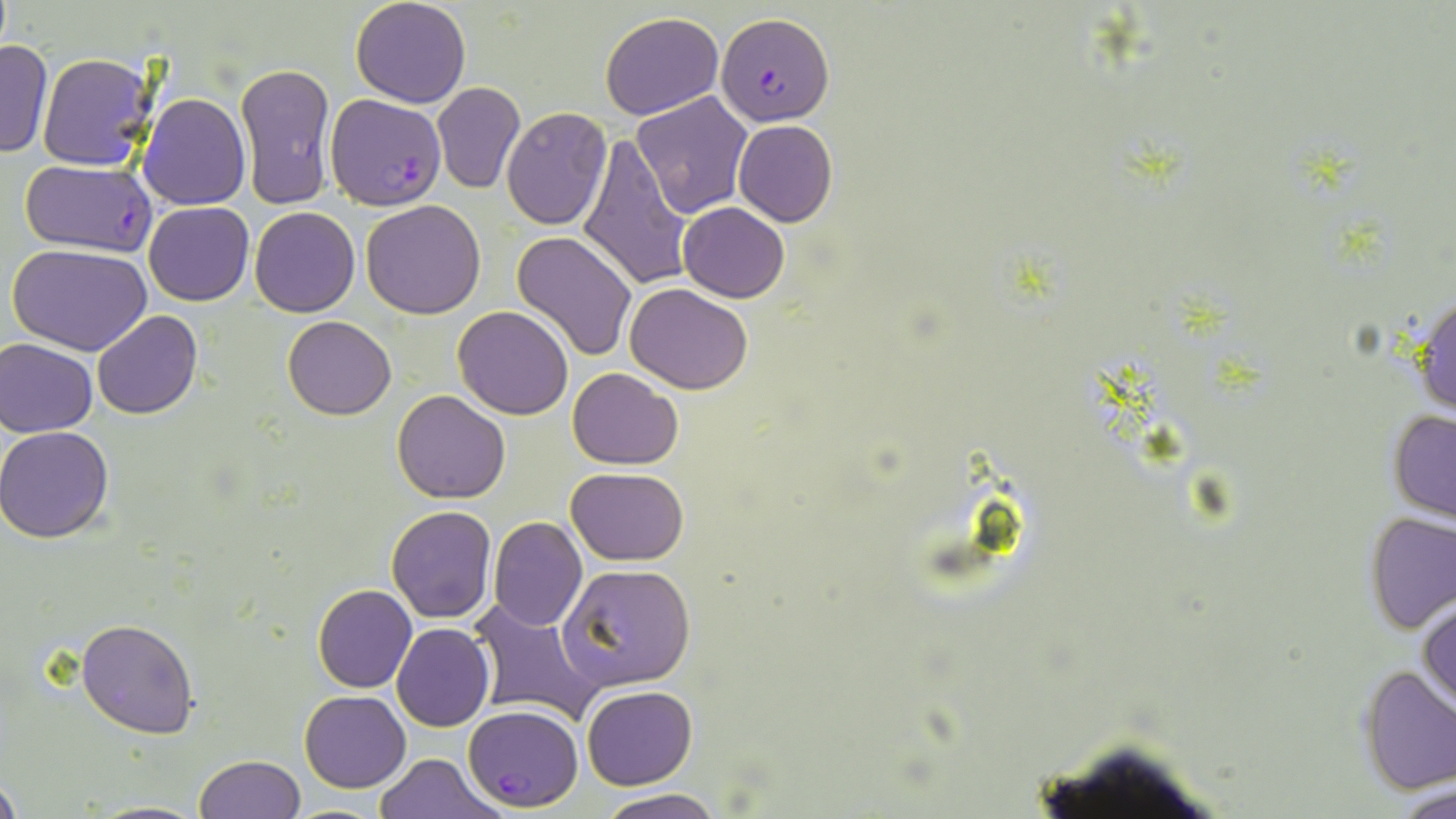
Summary:
  - Coordinate format: approximate bounding boxes as (x1,y1)-(x2,y2) corner pairs in pixels
  - Plasmodium falciparum-infected red blood cell locations: (716,11)-(834,126), (326,92)-(446,209), (18,159)-(159,254), (463,705)-(585,811)
  - Uninfected red blood cell locations: (350,0)-(471,108), (600,11)-(725,120), (0,40)-(52,158), (37,53)-(158,172), (236,62)-(336,211), (433,82)-(526,194), (633,90)-(752,219), (137,93)-(251,209), (501,108)-(611,228), (733,117)-(838,227), (578,135)-(693,291), (143,200)-(254,305), (361,200)-(486,319), (679,203)-(790,302), (249,207)-(360,317), (510,229)-(638,362), (8,242)-(154,354), (625,283)-(753,394), (1411,289)-(1455,419), (452,306)-(575,420), (93,311)-(202,420), (282,316)-(395,419), (1,339)-(98,437), (567,367)-(683,469), (391,389)-(510,503), (1387,408)-(1456,523), (0,426)-(114,542), (566,467)-(689,564), (386,505)-(497,623), (1364,511)-(1455,633), (489,516)-(587,632), (558,564)-(696,690), (313,584)-(417,692), (1419,597)-(1455,713), (466,599)-(607,729), (76,617)-(198,738), (392,623)-(493,731), (1357,664)-(1456,795), (581,685)-(697,788), (301,690)-(411,792), (372,752)-(503,818), (194,754)-(306,818), (0,773)-(22,819), (1395,782)-(1456,819), (596,789)-(726,819), (86,800)-(212,818), (277,803)-(396,819)
  - Slide-level diagnosis: Plasmodium falciparum
  - Field of view: one of a larger specimen
  - Magnification: 1000x
  - Image size: 1456×819 pixels
  - Preparation: thin blood smear
  - Stain: May-Grünwald-Giemsa
  - Modality: light microscopy